Point out each leukocyte.
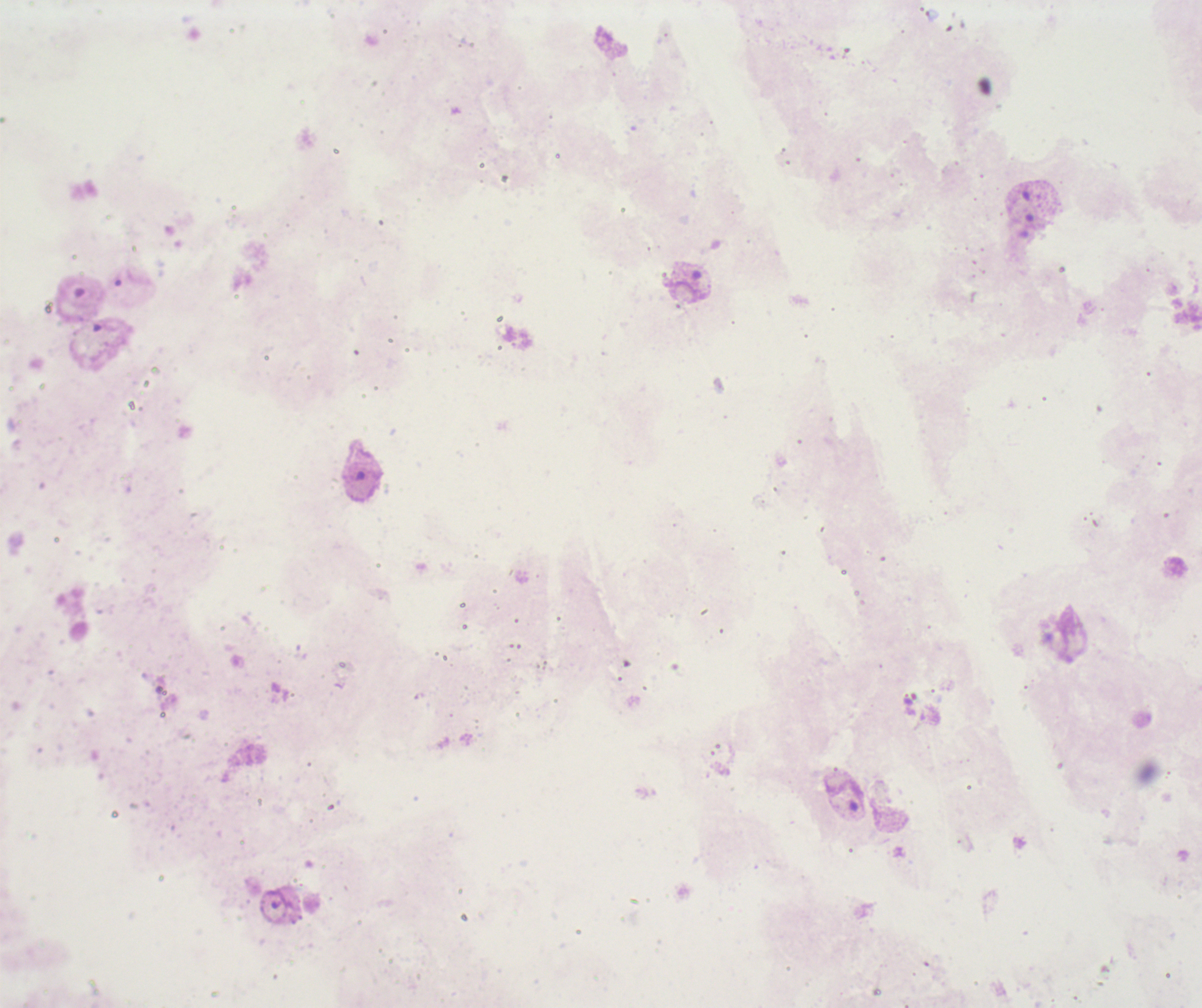
No leukocytes visible.

Approximate centers as [x, y] in pixels. Trophozoite locations: [685, 280]. Image is 1202×1008 pixels. Previously used in an actual diagnosis. One field from this slide. Background quality: unsatisfactory. 100x magnification. Thick smear of blood. Coloration quality: bad. Result: Plasmodium parasites detected. Romanowsky stain.